Report the malaria status of this cell.
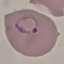
It is parasitized.

preparation = thin blood film
image type = cell patch, automatically extracted from a larger field of view and resized to 64 × 64 pixels
capture = smartphone through the microscope eyepiece
stain = Giemsa